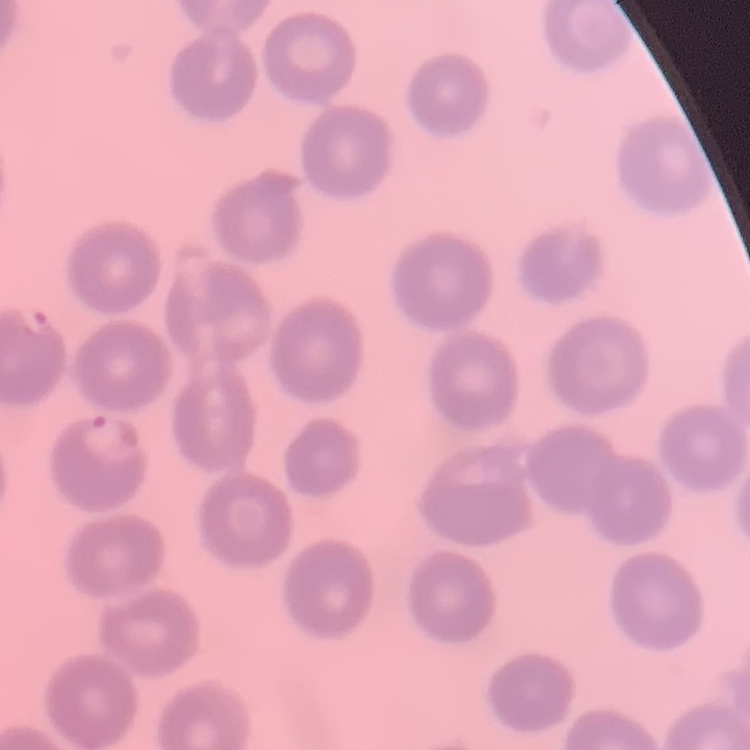 The erythrocytes exhibit no rouleaux formation. Thin blood film. Field's or Giemsa stain. One tile cut from a larger photomicrograph.